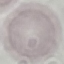

Summary:
  - Malaria status: uninfected
  - Preparation: thin blood smear
  - Capture: smartphone through the microscope eyepiece
  - Image type: automatically extracted cell patch, resized to 64 × 64 pixels
  - Stain: Giemsa